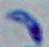

identification = Toxoplasma gondii
modality = photomicrograph
magnification = 1000x